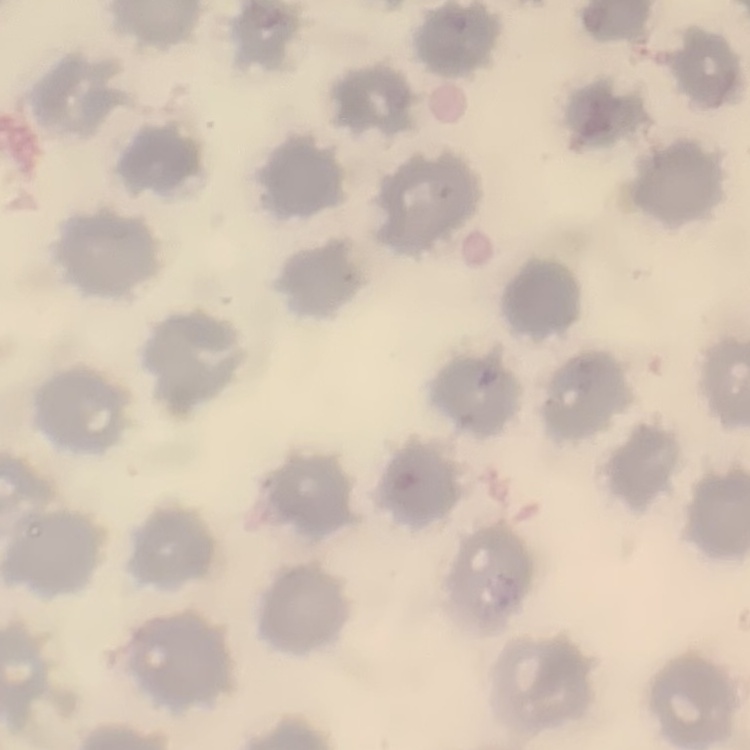
The red blood cells show no rouleaux formation. One tile cut from a larger photomicrograph. Thin blood smear. Stained with either Field's or Giemsa.